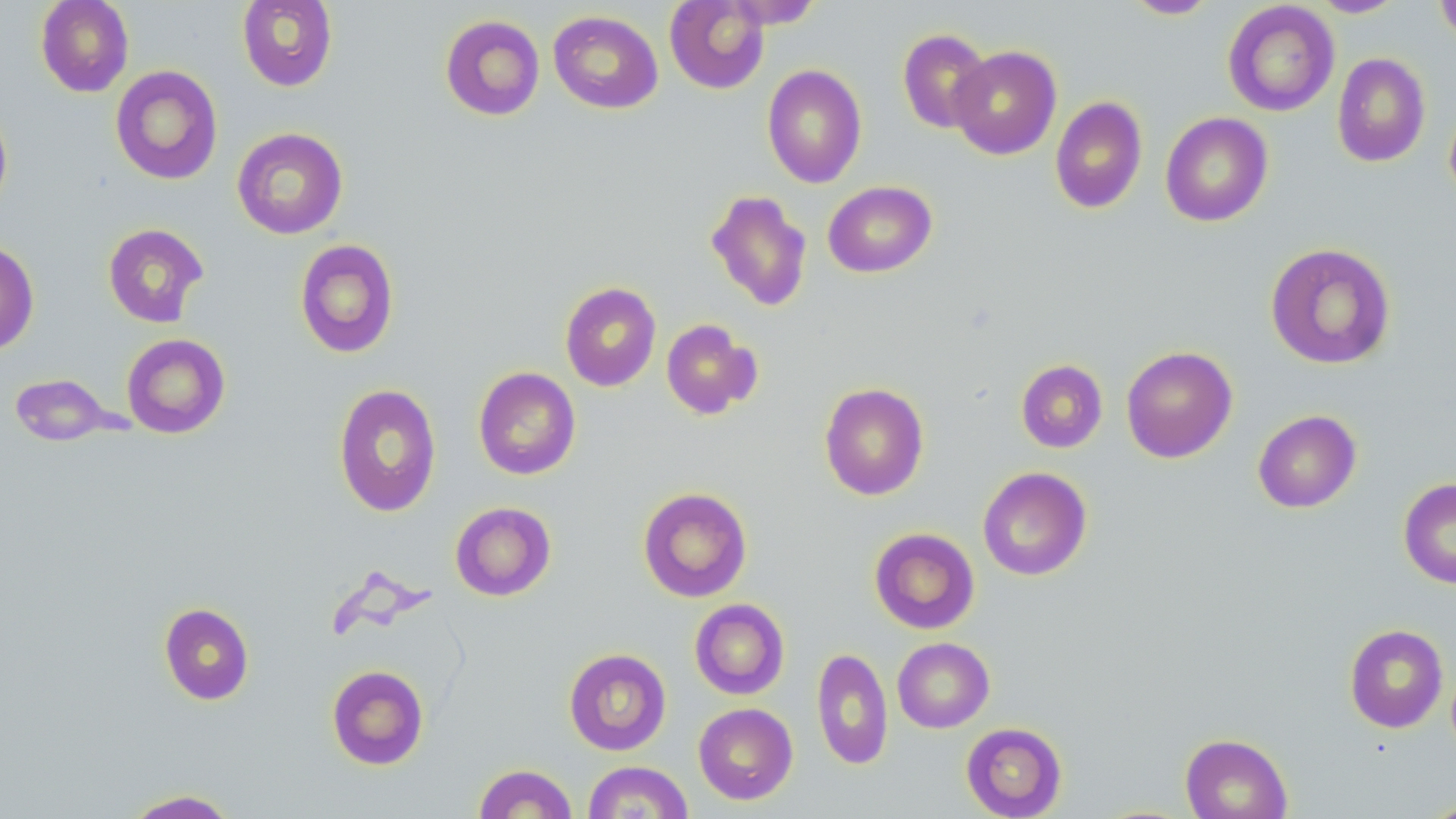
Summary:
  - Coordinate format: approximate bounding boxes as (x1, y1, x2, y2) in pixels
  - Uninfected red blood cell locations: (35, 0, 134, 97), (237, 0, 337, 91), (1123, 0, 1219, 19), (1309, 0, 1408, 18), (1434, 0, 1456, 46), (664, 1, 770, 94), (723, 1, 824, 28), (1222, 2, 1340, 117), (548, 10, 663, 114), (440, 14, 545, 121), (897, 28, 993, 134), (949, 45, 1062, 160), (1332, 52, 1431, 168), (761, 64, 867, 189), (110, 65, 223, 185), (1049, 96, 1148, 214), (1444, 98, 1456, 207), (0, 102, 13, 215), (1160, 112, 1273, 227), (231, 127, 348, 239), (822, 180, 937, 278), (706, 189, 813, 312), (102, 223, 210, 327), (0, 239, 39, 355), (294, 239, 399, 358), (1265, 242, 1396, 370), (560, 282, 661, 391), (660, 318, 762, 420), (121, 333, 231, 438), (1121, 346, 1237, 463), (1016, 360, 1108, 453), (473, 366, 581, 480), (8, 373, 120, 446), (819, 382, 929, 500), (332, 383, 442, 518), (1252, 409, 1362, 513), (978, 466, 1092, 581), (1398, 477, 1456, 589), (638, 486, 753, 602), (450, 501, 556, 601), (869, 527, 980, 634), (689, 598, 790, 700), (158, 602, 255, 705), (1344, 624, 1449, 733), (892, 637, 994, 733), (811, 647, 893, 770), (564, 648, 672, 756), (326, 665, 429, 770), (693, 703, 798, 805), (960, 722, 1067, 818), (1180, 733, 1292, 819), (582, 761, 694, 819), (473, 763, 578, 818), (122, 789, 240, 818)
  - Slide-level diagnosis: negative for blood parasites
  - Field of view: one of a larger specimen
  - Modality: optical microscopy
  - Preparation: thin blood smear
  - Magnification: 1000x
  - Stain: May-Grünwald-Giemsa
  - Image size: 1456×819 pixels